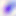

Summary:
  - Magnification: 400x
  - Modality: photomicrograph
  - Identification: Toxoplasma gondii